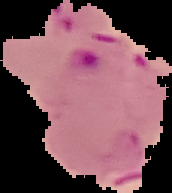

Summary:
  - Image size: 172×193 pixels
  - Result: malaria parasites detected
  - Preparation: thin blood smear
  - Image type: segmented cell region on a black background